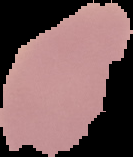

image type = segmented cell region with the area outside set to black
preparation = thin blood smear
image size = 133×157 pixels
malaria status = uninfected